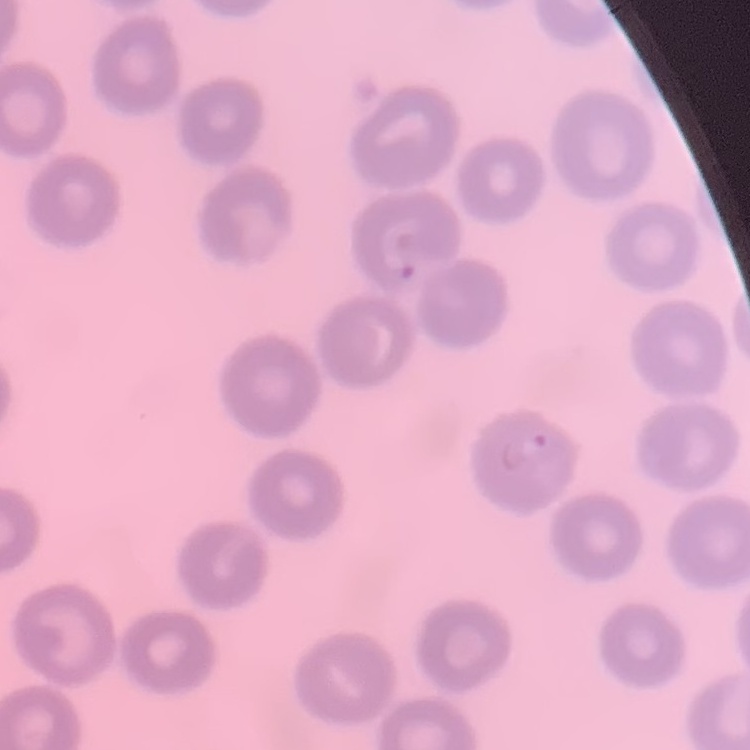

The red blood cells exhibit no rouleaux formation. Thin blood smear. Field's or Giemsa stain. One tile cut from a larger photomicrograph.